Outline every parasitised red blood cell.
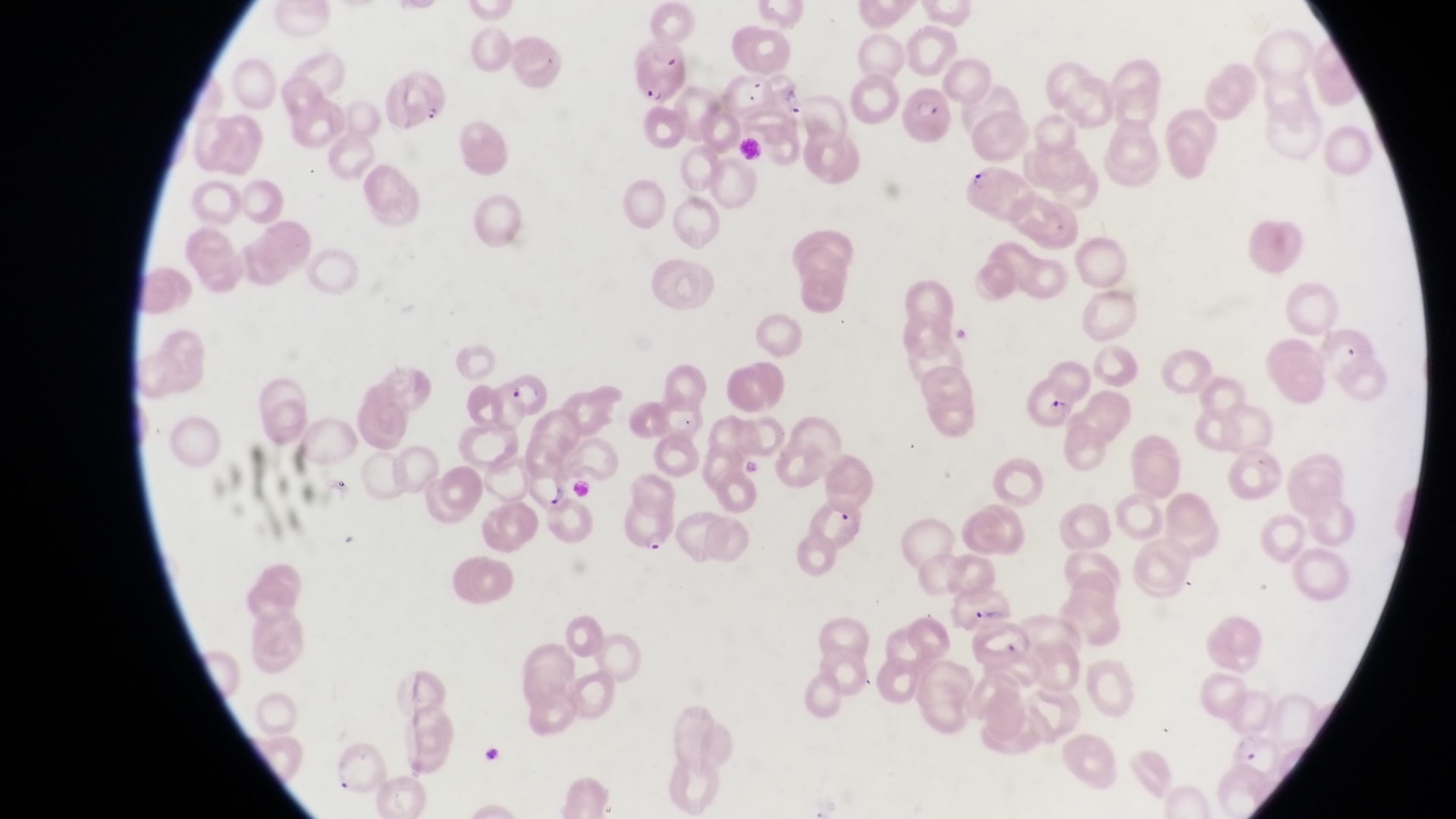

Approximate bounding boxes as left top right bottom in pixels.
Parasitised red blood cells: 631 50 692 102; 384 73 448 128; 904 85 954 146; 962 164 1038 224; 502 369 552 419; 1021 376 1081 429; 523 459 575 518; 620 495 680 556.

capture = smartphone photograph through the eyepiece of an Olympus CX-23 microscope
image size = 1456×819 pixels
magnification = 1000x
preparation = thin blood smear
field of view = single
country = Uganda